Comment on the morphology of the red blood cells.
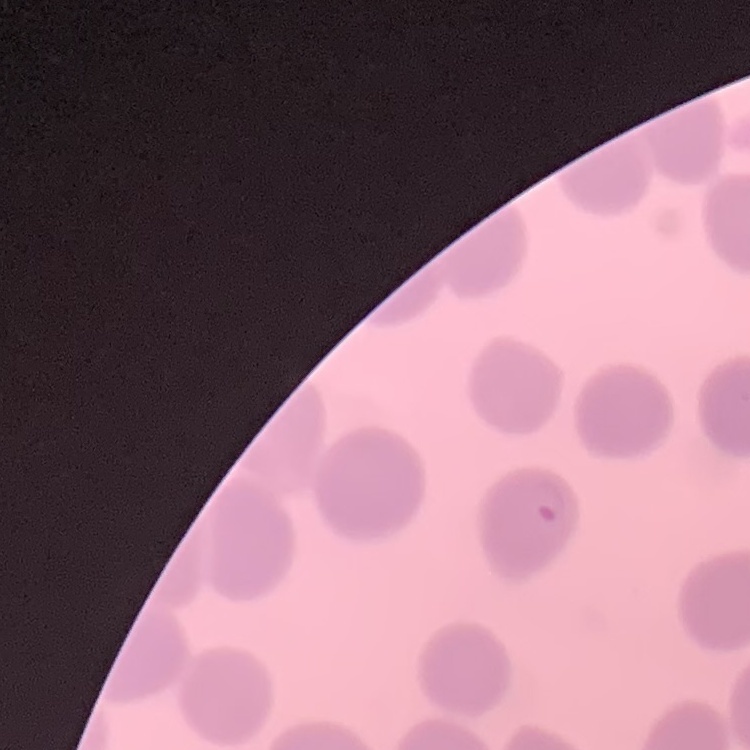
They show no rouleaux formation.

Summary:
  - Preparation: thin peripheral smear
  - Stain: Field's or Giemsa
  - Image type: square crop of a larger photomicrograph